Identify the parasite.
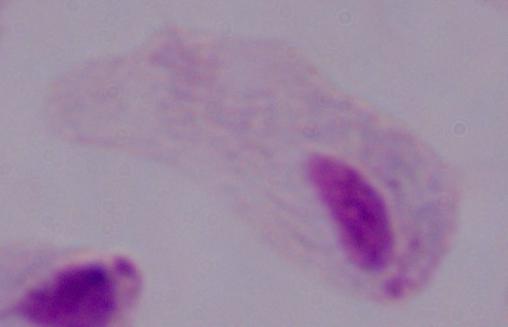
This is a trichomonad.

magnification = 1000x
modality = micrograph